Describe the morphology of the erythrocytes.
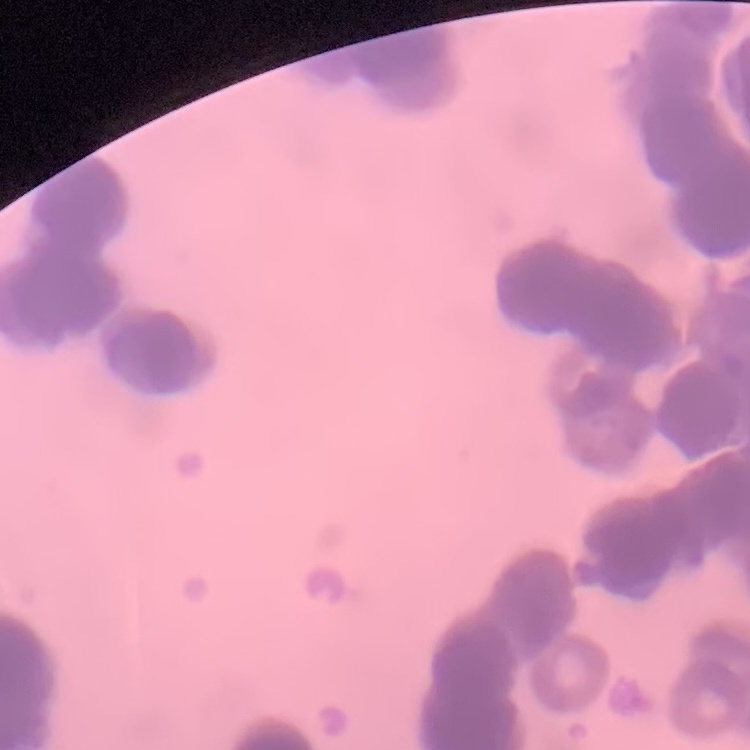
They show rouleaux formation.

Summary:
  - Preparation: thin blood smear
  - Image type: square crop of a larger photomicrograph
  - Stain: Field's or Giemsa